Comment on the morphology of the erythrocytes.
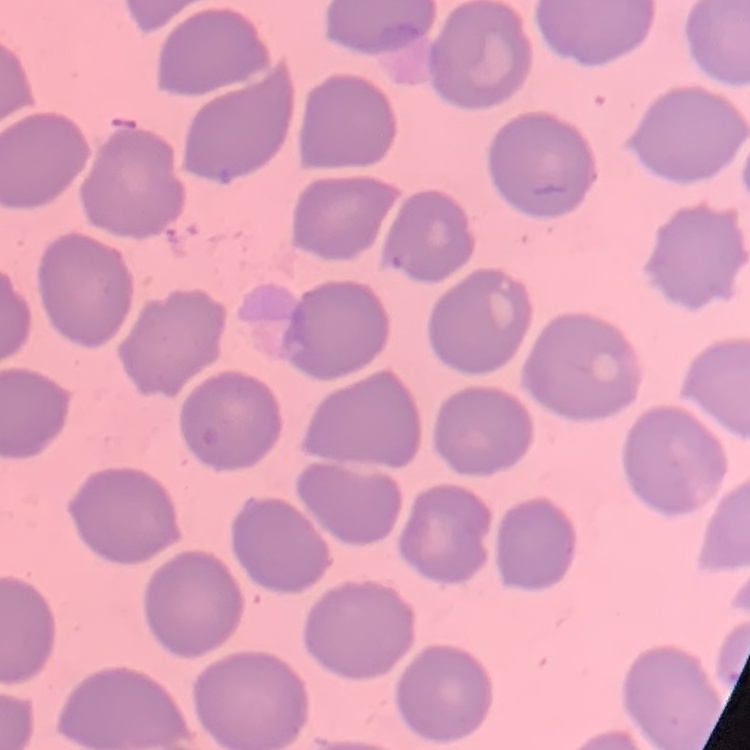
No rouleaux formation.

Summary:
  - Image type: one tile cut from a larger photomicrograph
  - Stain: Field's or Giemsa
  - Preparation: thin peripheral smear